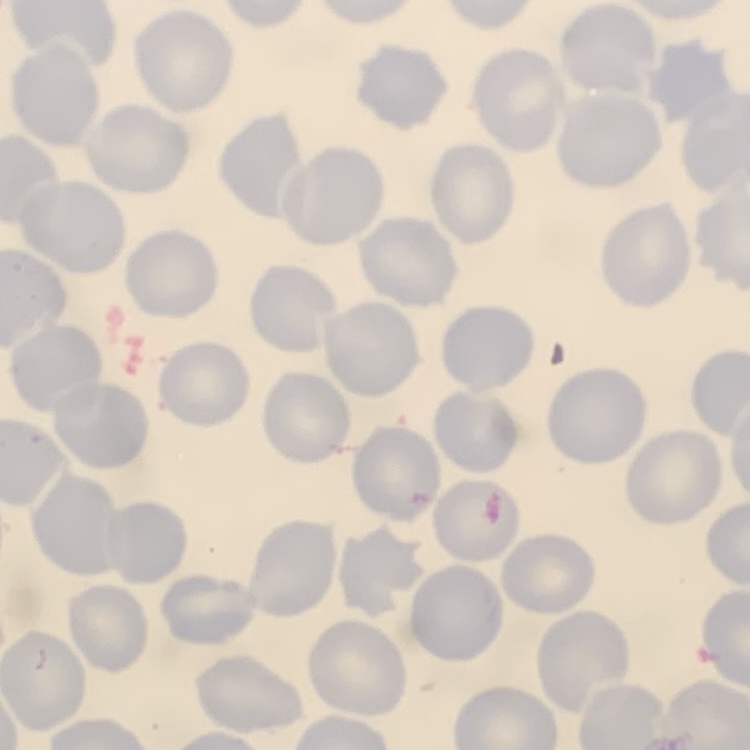
The erythrocytes exhibit no rouleaux formation. Square crop of a larger photomicrograph. Thin peripheral smear. Stained with either Field's or Giemsa.